State which cell type is depicted.
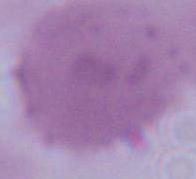
This is an erythrocyte.

Summary:
  - Magnification: 1000x
  - Modality: photomicrograph